Describe the morphology of the red blood cells.
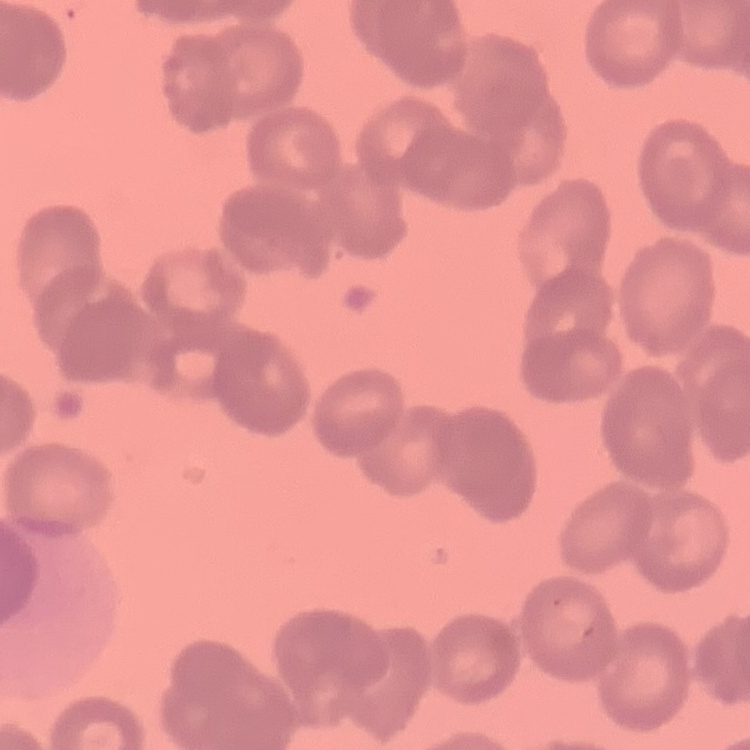
Rouleaux formation.

Summary:
  - Preparation: thin blood smear
  - Stain: Field's or Giemsa
  - Image type: one tile cut from a larger photomicrograph